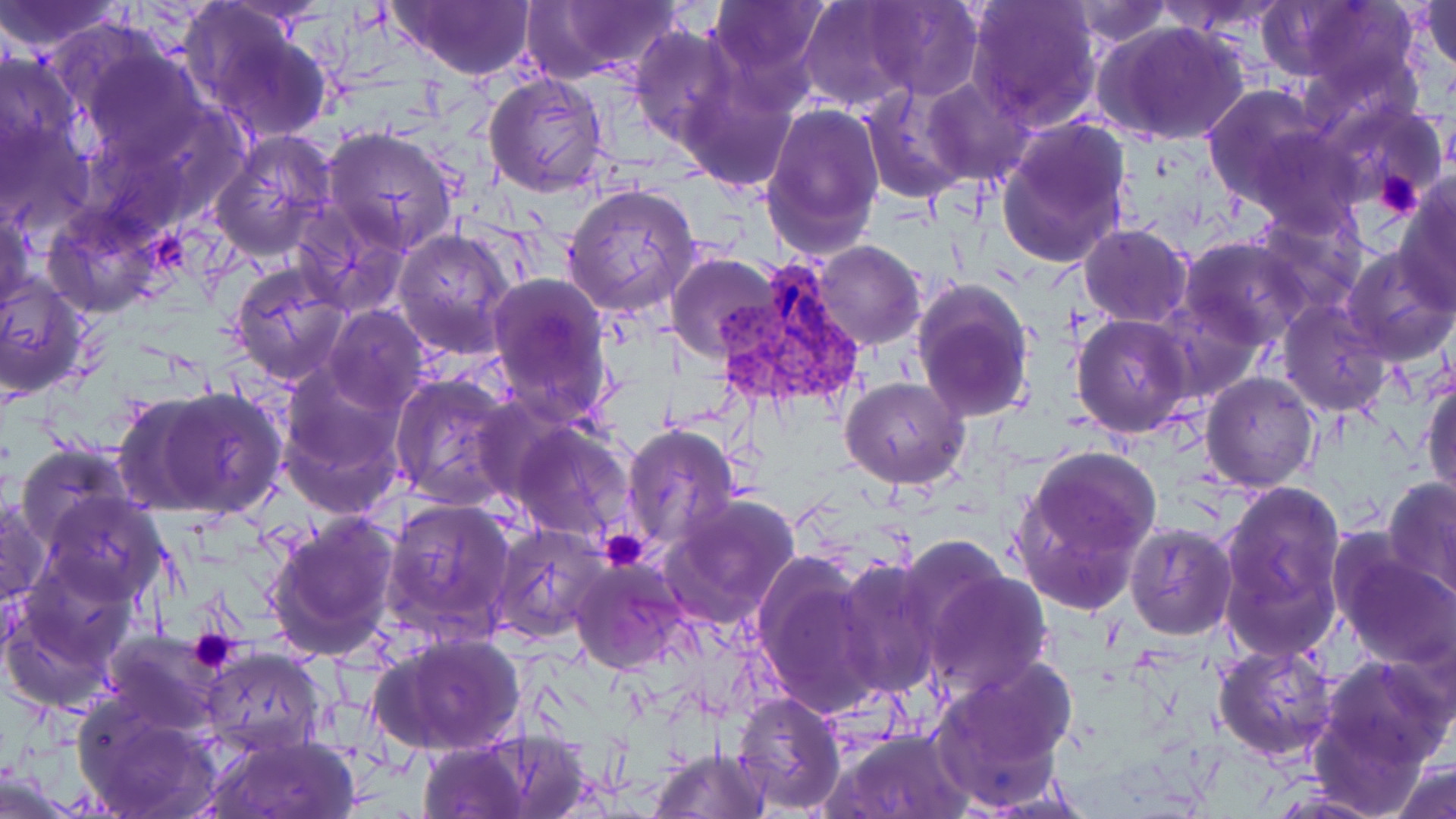

Approximate bounding boxes as [x1, y1, x2, y2] in pixels. Plasmodium vivax-infected red blood cell locations: [714, 256, 864, 408]. Platelet locations: [1375, 170, 1426, 219], [153, 229, 193, 277], [600, 527, 652, 573], [185, 629, 243, 677]. Uninfected red blood cell locations: [391, 0, 538, 79], [706, 0, 829, 94], [864, 0, 984, 100], [965, 0, 1103, 131], [1152, 0, 1286, 40], [1421, 0, 1456, 78], [0, 1, 132, 54], [543, 1, 686, 79], [795, 1, 922, 112], [1067, 1, 1170, 48], [1263, 1, 1423, 104], [183, 5, 336, 143], [1096, 19, 1250, 146], [629, 27, 738, 145], [72, 44, 208, 168], [0, 48, 87, 178], [483, 71, 610, 197], [676, 75, 798, 192], [920, 78, 1031, 186], [1204, 84, 1328, 209], [859, 88, 969, 202], [1320, 99, 1449, 210], [761, 103, 885, 257], [0, 115, 95, 235], [995, 118, 1133, 269], [322, 125, 463, 254], [1246, 128, 1363, 234], [209, 131, 338, 260], [1394, 175, 1456, 309], [562, 183, 701, 319], [0, 200, 36, 317], [292, 204, 412, 317], [43, 205, 166, 317], [1253, 208, 1367, 316], [1080, 223, 1192, 327], [391, 229, 517, 357], [1180, 238, 1312, 348], [810, 241, 926, 351], [1340, 244, 1456, 366], [667, 253, 782, 363], [229, 261, 352, 386], [487, 271, 614, 420], [1, 274, 90, 400], [910, 278, 1035, 424], [1156, 299, 1263, 404], [1277, 299, 1393, 419], [324, 306, 430, 413], [1071, 314, 1195, 440], [275, 366, 413, 518], [388, 372, 519, 506], [1200, 372, 1320, 493], [1422, 372, 1455, 504], [841, 377, 969, 489], [121, 385, 288, 522], [472, 395, 569, 503], [510, 421, 636, 540], [621, 425, 741, 551], [17, 441, 137, 549], [1012, 447, 1161, 611], [1383, 476, 1456, 600], [1218, 478, 1346, 654], [37, 491, 166, 606], [659, 494, 801, 628], [0, 495, 49, 610], [382, 496, 519, 644], [263, 510, 403, 660], [489, 521, 609, 644], [1125, 524, 1236, 640], [1334, 545, 1456, 670], [750, 551, 883, 720], [834, 558, 945, 702], [570, 560, 692, 674], [2, 564, 135, 712], [917, 565, 1054, 699], [379, 632, 524, 758], [103, 634, 224, 734], [1212, 643, 1339, 763], [199, 648, 327, 756], [1313, 653, 1453, 787], [930, 661, 1078, 807], [730, 689, 847, 813], [72, 694, 222, 819], [459, 726, 600, 818], [825, 727, 975, 818], [204, 731, 360, 818], [415, 738, 532, 819], [646, 745, 768, 819], [1388, 760, 1455, 819], [0, 769, 85, 819]. Slide-level diagnosis: Plasmodium vivax. Single field of view. Captured at 1000x magnification. Thin blood film. May-Grünwald-Giemsa stain. Image is 1456×819 pixels. Optical microscopy.